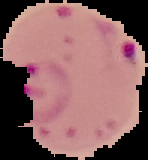

preparation = thin blood smear
malaria status = parasitized
image size = 148×160 pixels
image type = segmented cell region with the area outside set to black